Give a bounding box for every malaria parasite.
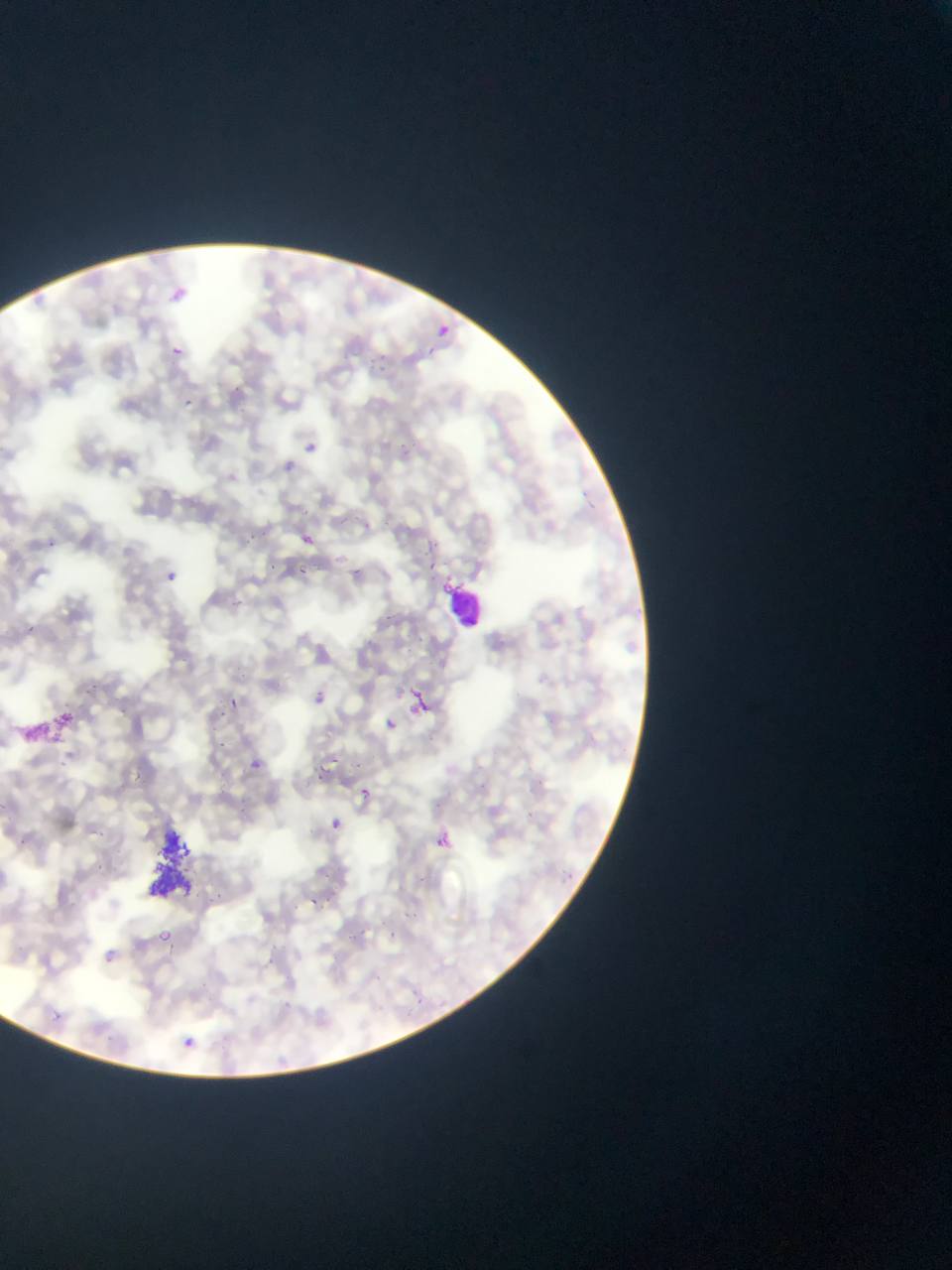

Approximate bounding boxes as (left, top, right, bottom) in pixels.
Malaria parasites: (169, 281, 195, 302), (437, 318, 464, 337), (426, 342, 449, 362), (171, 344, 182, 355), (186, 395, 195, 411), (304, 439, 318, 455), (286, 446, 304, 482), (358, 520, 371, 534), (243, 531, 257, 542), (296, 531, 317, 550), (44, 537, 53, 551), (428, 558, 444, 577), (265, 562, 279, 577), (349, 564, 366, 580), (297, 567, 308, 578), (161, 568, 181, 586), (24, 622, 42, 636), (83, 674, 98, 695), (309, 686, 331, 708), (402, 686, 436, 723), (227, 694, 241, 716), (217, 706, 228, 721), (377, 714, 403, 738), (216, 740, 231, 751), (54, 757, 74, 769), (351, 760, 368, 773), (251, 761, 260, 773), (319, 765, 327, 776), (137, 772, 146, 783), (353, 783, 375, 802), (524, 810, 540, 824), (324, 815, 347, 836), (430, 829, 455, 854), (95, 831, 107, 846), (321, 869, 338, 879), (309, 898, 320, 909), (406, 909, 422, 921), (149, 925, 179, 951), (390, 930, 410, 944), (268, 953, 279, 969), (410, 992, 431, 1016), (51, 1004, 65, 1024), (171, 1030, 205, 1059).

Leukocyte locations: (444, 581, 487, 632). Artifact (stain precipitate or debris) locations: (10, 696, 83, 739), (144, 819, 227, 893). Photographed through a microscope with a mobile-phone camera. Collected in Ghana. Thin blood film. Single field of view. Image is 952×1270 pixels.